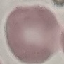

malaria_status: uninfected
capture: smartphone through the microscope eyepiece
stain: Giemsa
image_type: cell patch, automatically extracted from a larger field of view and resized to 64 × 64 pixels
preparation: thin blood film